Mark where platelets are.
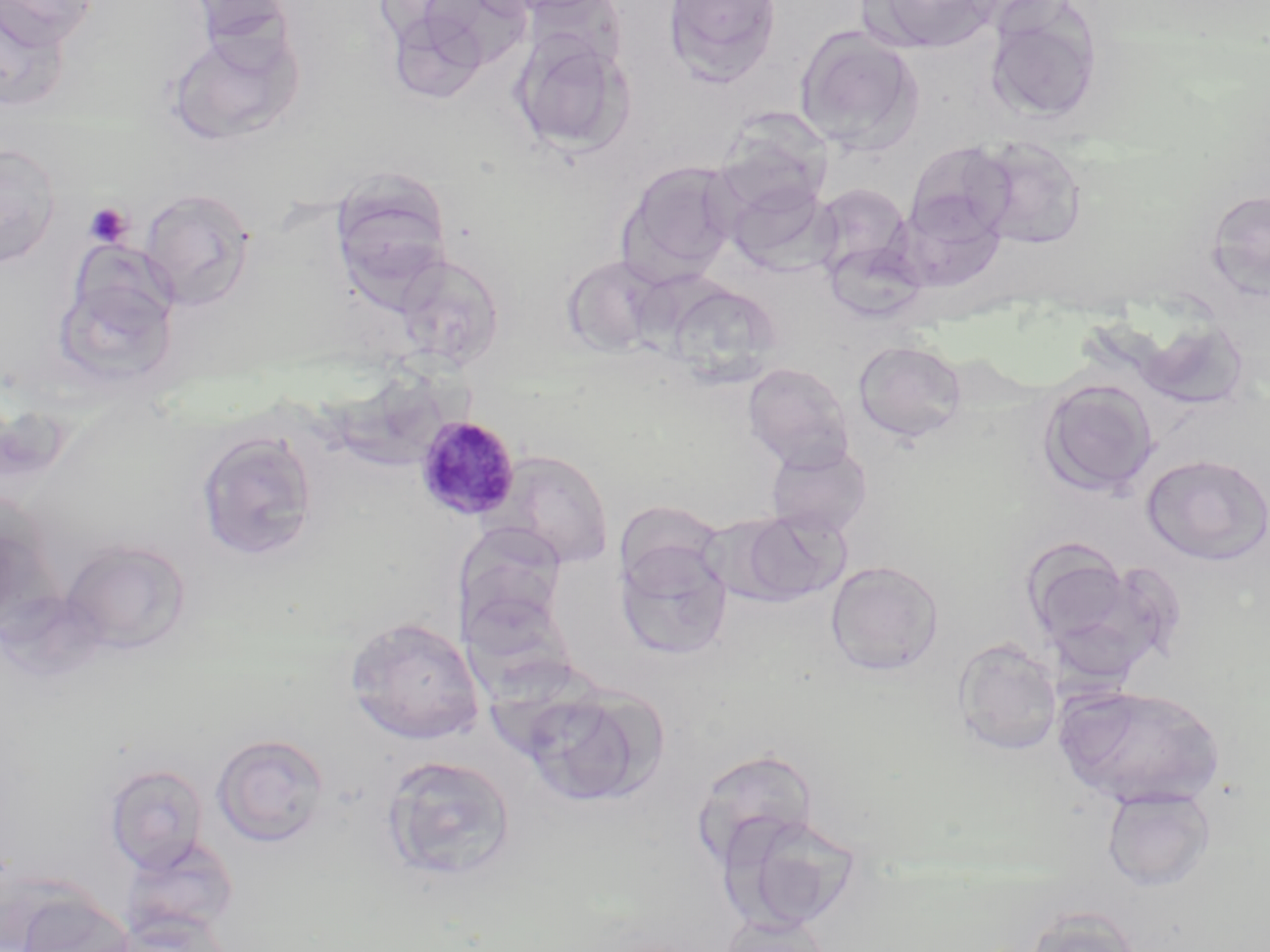

Approximate bounding boxes as [x1, y1, x2, y2] in pixels.
Platelets: [84, 202, 132, 247].

Uninfected red blood cell locations: [1, 0, 101, 45], [183, 0, 300, 51], [406, 0, 532, 81], [663, 0, 781, 85], [863, 0, 999, 54], [0, 3, 71, 112], [984, 3, 1103, 126], [384, 8, 492, 104], [794, 26, 924, 157], [165, 27, 305, 145], [509, 28, 633, 156], [715, 108, 833, 216], [971, 136, 1087, 250], [905, 141, 1017, 245], [0, 142, 62, 268], [621, 161, 740, 277], [724, 176, 837, 274], [812, 183, 914, 279], [332, 185, 451, 303], [139, 188, 256, 310], [1205, 188, 1270, 299], [824, 237, 929, 323], [394, 251, 505, 371], [562, 255, 667, 357], [53, 268, 178, 391], [665, 282, 785, 387], [1136, 317, 1251, 411], [853, 340, 967, 444], [742, 362, 855, 471], [1038, 379, 1159, 498], [195, 430, 319, 561], [765, 441, 873, 539], [491, 448, 615, 569], [1140, 454, 1270, 566], [1, 491, 59, 633], [733, 508, 850, 607], [60, 538, 192, 655], [1019, 540, 1153, 669], [615, 541, 733, 660], [825, 560, 944, 677], [345, 615, 485, 744], [953, 638, 1063, 756], [1054, 683, 1228, 809], [520, 685, 663, 808], [212, 733, 330, 847], [690, 747, 820, 869], [381, 755, 517, 882], [104, 763, 209, 873], [1101, 785, 1216, 892], [723, 812, 865, 933], [122, 836, 240, 939], [12, 892, 135, 952], [1022, 905, 1145, 952], [714, 916, 832, 952]. Plasmodium malariae-infected red blood cell locations: [415, 414, 521, 520]. Slide-level diagnosis: Plasmodium malariae. Optical microscopy. Image is 1270×952 pixels. 1000x magnification. May-Grünwald-Giemsa stain. Thin blood smear. Single field of view.